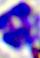

{
  "modality": "micrograph",
  "identification": "white blood cell",
  "magnification": "400x"
}